Comment on the morphology of the erythrocytes.
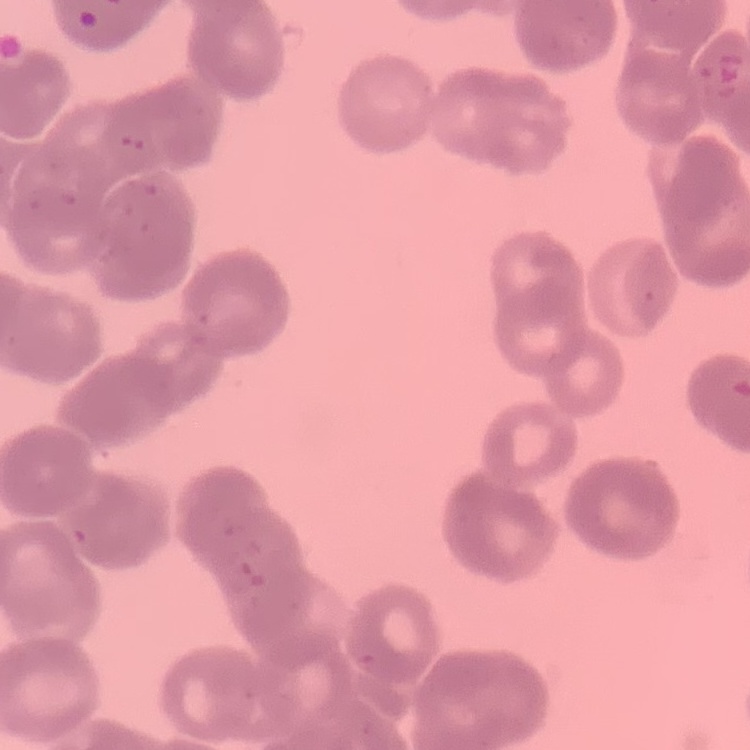
They show rouleaux formation.

image type = square crop of a larger photomicrograph
preparation = thin peripheral smear
stain = Field's or Giemsa